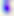 Photomicrograph. Toxoplasma gondii is shown. Captured at 400x magnification.